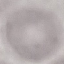

Summary:
  - Malaria status: uninfected
  - Capture: smartphone camera at the microscope eyepiece
  - Stain: Giemsa
  - Image type: automatically extracted cell patch, resized to 64 × 64 pixels
  - Preparation: thin blood film